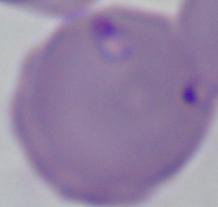

Summary:
  - Identification: Babesia
  - Magnification: 1000x
  - Modality: photomicrograph